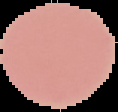
Summary:
  - Image type: segmented cell region on a black background
  - Preparation: thin blood smear
  - Image size: 118×112 pixels
  - Malaria status: uninfected